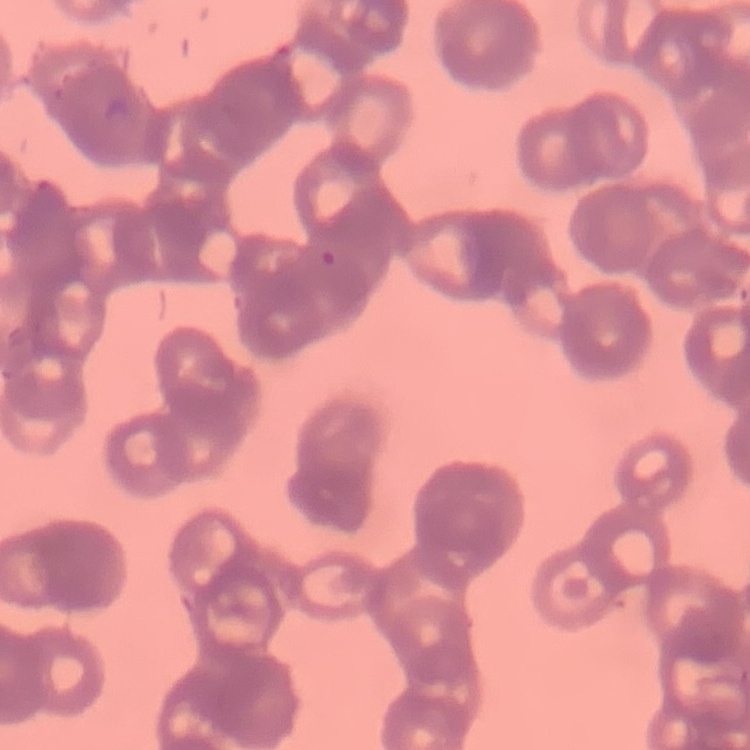

red_blood_cell_morphology: rouleaux formation
image_type: one tile cut from a larger photomicrograph
preparation: thin blood film
stain: Field's or Giemsa